Comment on the morphology of the red blood cells.
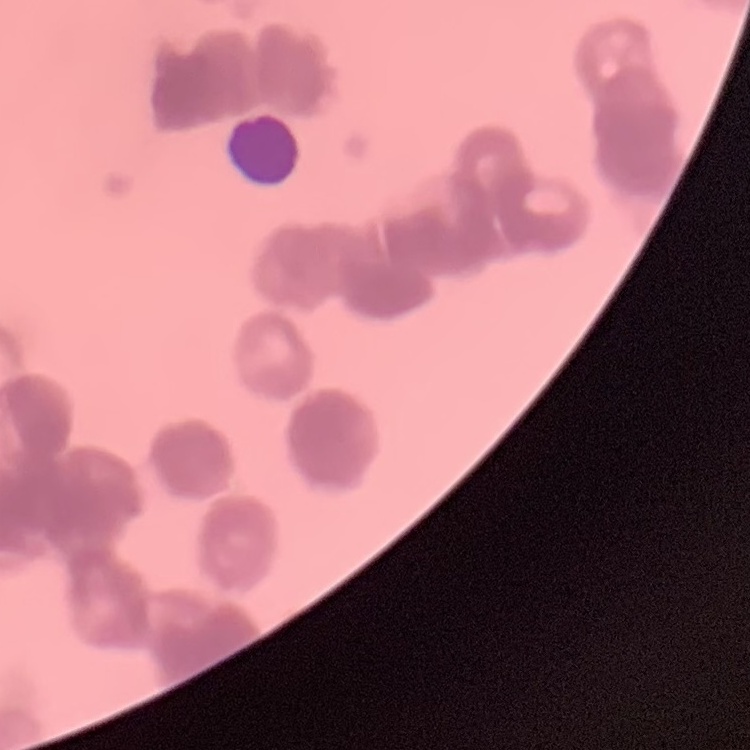
They show rouleaux formation.

Summary:
  - Preparation: thin blood film
  - Image type: square crop of a larger photomicrograph
  - Stain: Field's or Giemsa